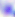
Captured at 400x magnification. Micrograph. Toxoplasma gondii is shown.